Report the malaria status of this cell.
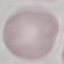

Uninfected.

Summary:
  - Stain: Giemsa
  - Image type: automatically extracted cell patch, resized to 64 × 64 pixels
  - Preparation: thin smear
  - Capture: smartphone through the microscope eyepiece